Report the malaria status of this cell.
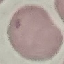
It is uninfected.

stain = Giemsa
capture = smartphone camera at the microscope eyepiece
image type = cell patch, automatically extracted from a larger field of view and resized to 64 × 64 pixels
preparation = thin blood smear